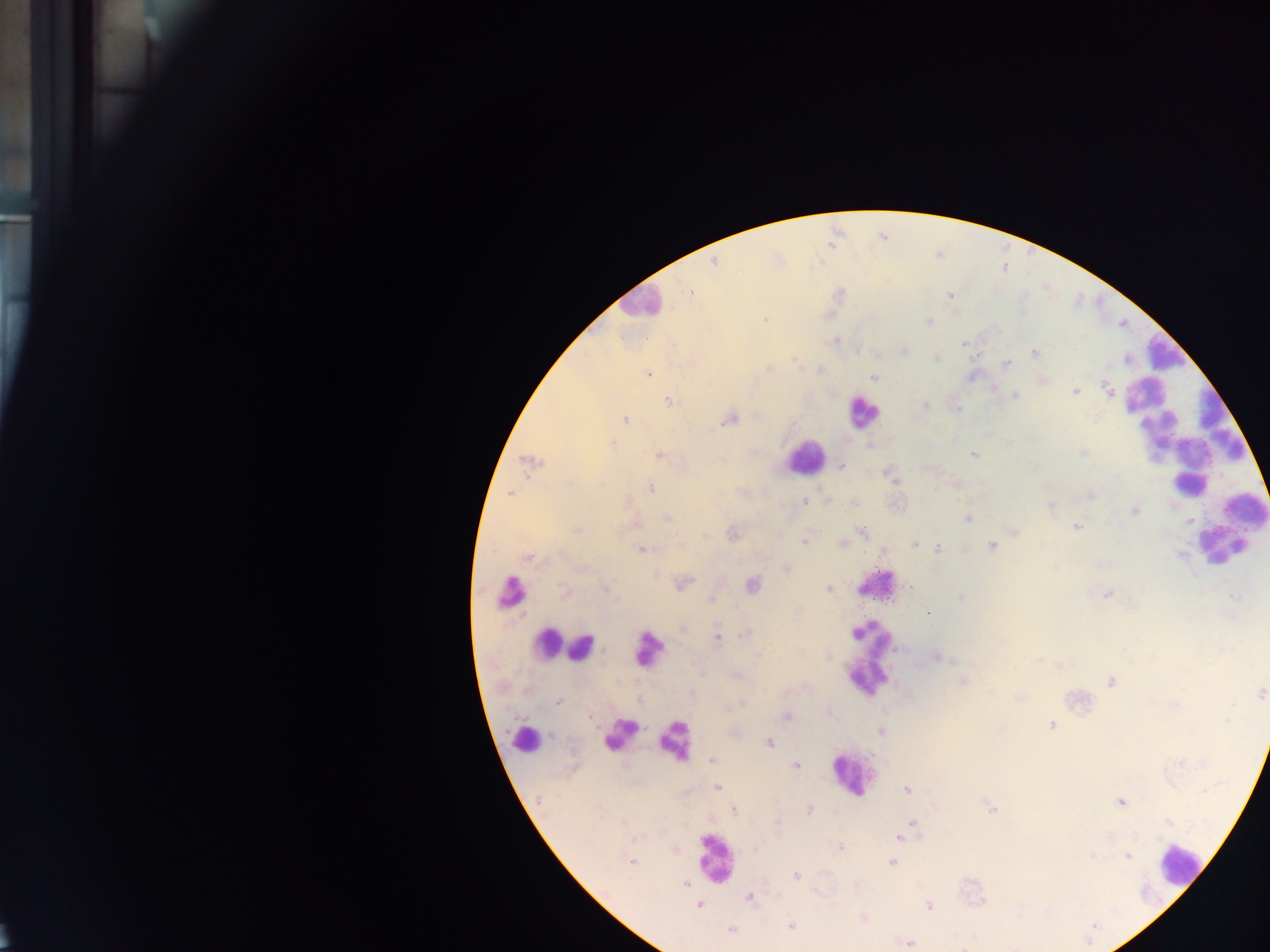
Approximate centers as x y in pixels.
Summary:
  - Leukocyte locations: 639 303; 862 411; 1189 439; 804 456; 1222 546; 875 585; 511 591; 873 634; 550 645; 584 646; 645 647; 865 676; 621 734; 527 739; 677 740; 853 775; 713 857; 1179 865
  - Plasmodium parasite locations: 714 262; 690 292; 950 295; 764 319; 928 320; 836 340; 964 343; 906 350; 1035 352; 936 358; 1007 363; 768 369; 649 373; 873 378; 1044 379; 1107 389; 1075 391; 1015 396; 668 400; 926 404; 957 409; 625 419; 731 419; 1008 444; 613 445; 1082 452; 973 454; 659 456; 530 462; 841 466; 892 477; 650 487; 511 494; 1090 494; 804 501; 854 502; 1051 506; 1134 511; 668 517; 969 518; 1077 527; 575 530; 863 531; 1016 532; 733 534; 805 541; 843 544; 915 544; 992 546; 938 548; 642 549; 528 557; 786 569; 684 582; 752 584; 607 589; 828 589; 564 591; 1107 594; 961 597; 1235 597; 711 599; 928 612; 683 628; 744 634; 718 638; 758 655; 937 657; 1038 659; 737 676; 963 682; 1111 683; 1260 693; 1019 697; 557 702; 742 704; 787 715; 1228 718; 1051 726; 881 731; 768 743; 712 760; 797 766; 717 786; 907 790; 1122 802; 992 809; 734 810; 810 811; 1170 823; 777 824; 912 824; 907 830; 902 836; 840 847; 1127 855; 631 861; 892 863; 797 875; 686 884; 750 897; 700 905; 929 906; 791 926; 731 929; 909 943
  - Image size: 1270×952 pixels
  - Capture: mobile-phone photograph through a microscope
  - Country: Ghana
  - Field of view: single
  - Preparation: thick blood smear